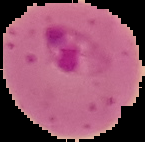

preparation = thin blood film
result = Plasmodium parasites identified
image size = 145×142 pixels
image type = segmented cell region with the area outside set to black